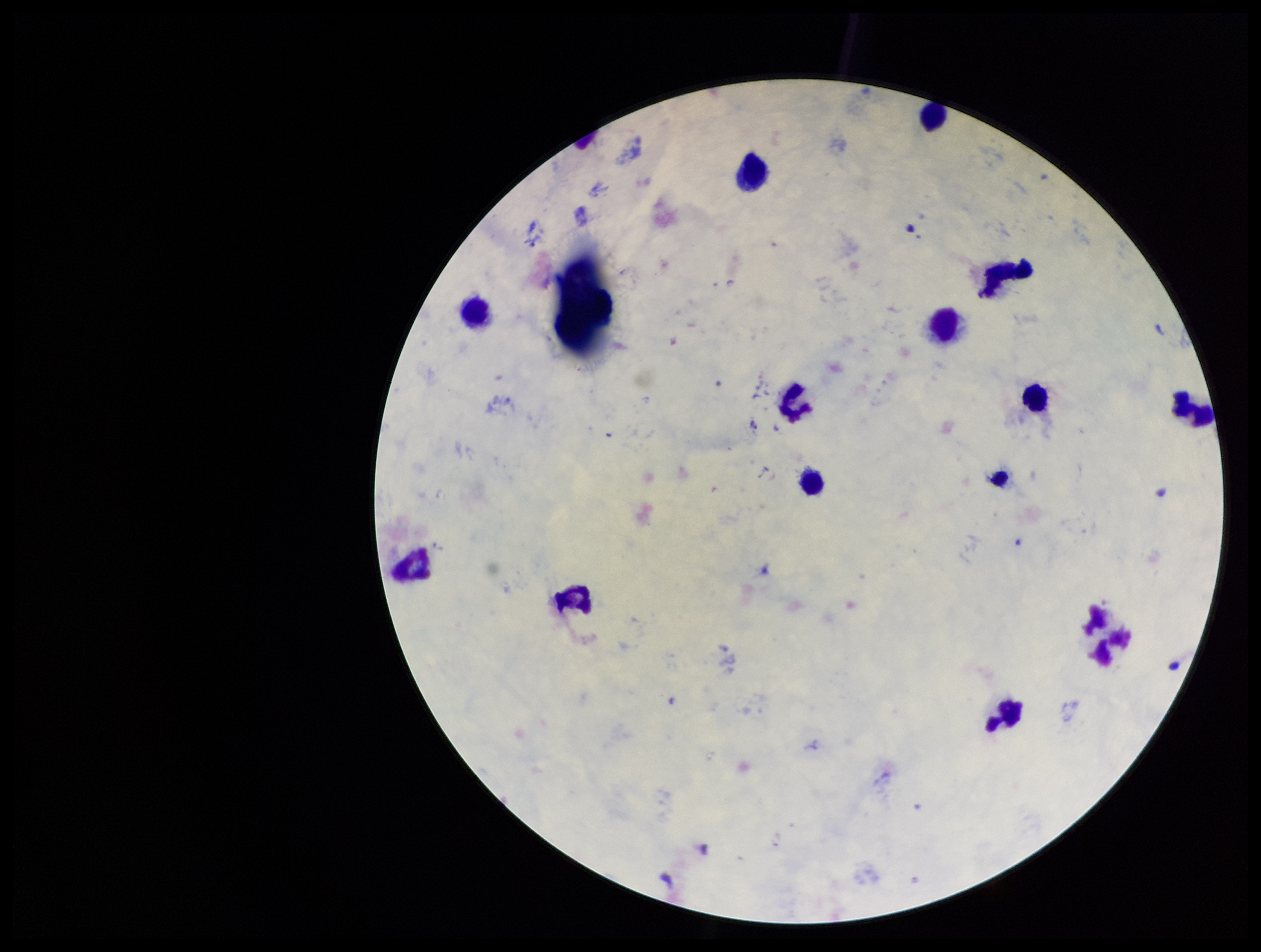

Summary:
  - Parasite count: 0
  - Image size: 1261×952 pixels
  - Species reported for this patient: Plasmodium vivax
  - Preparation: thick smear
  - Patient malaria status: positive
  - Plasmodium parasites: none seen
  - Stain: Giemsa
  - Leukocyte count: 11
  - Capture: smartphone photograph through the microscope eyepiece
  - Field of view: one from this slide